Describe the morphology of the red blood cells.
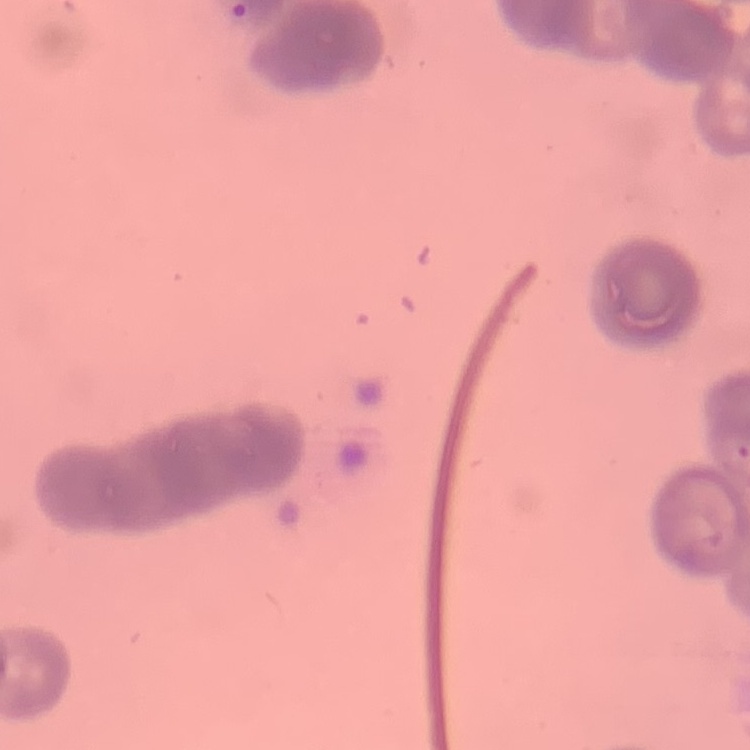
They show rouleaux formation.

One tile cut from a larger photomicrograph. Thin blood film. Stained with either Field's or Giemsa.